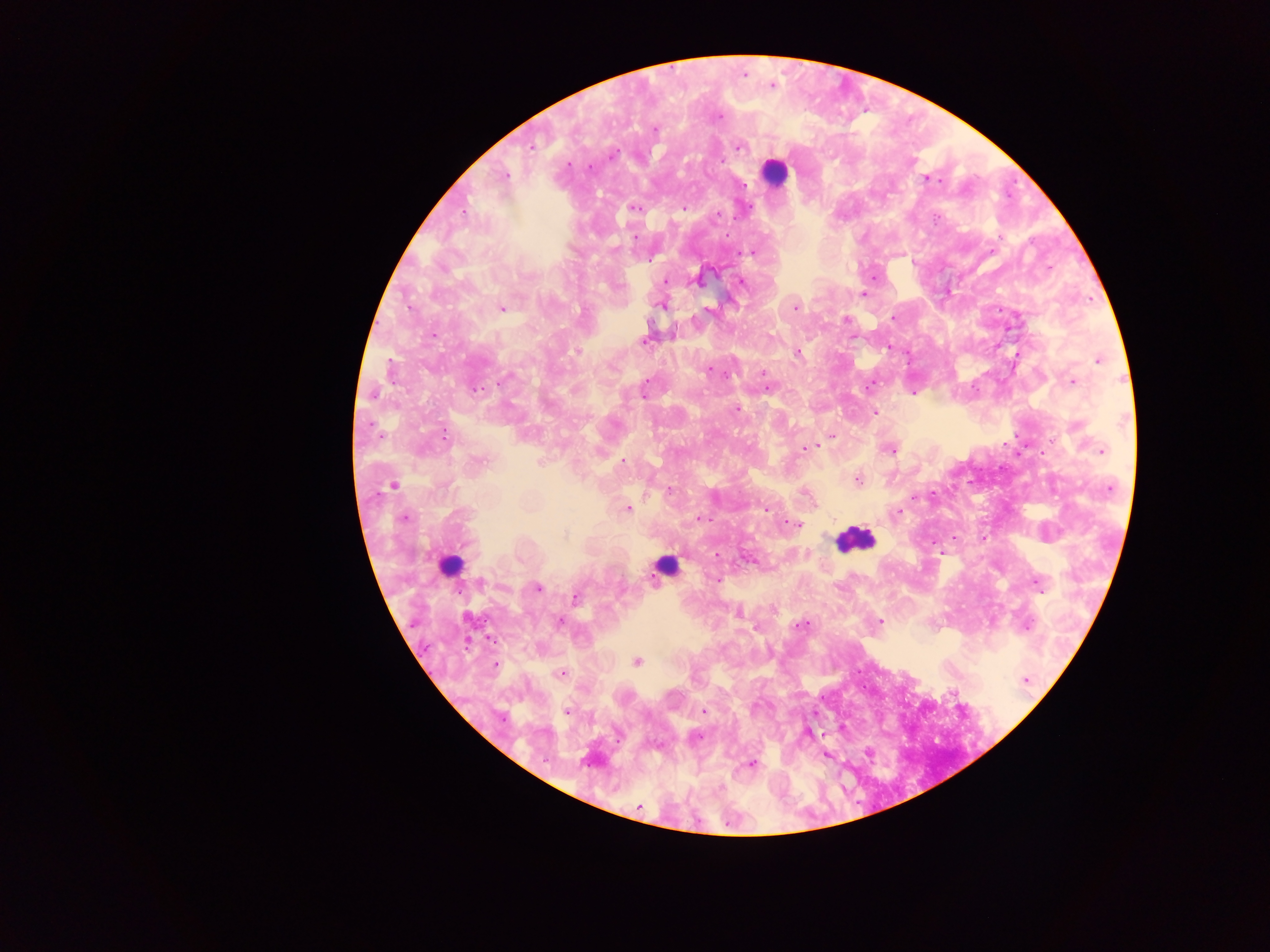
preparation = thick blood film
image size = 1270×952 pixels
field of view = single
country = Ghana
capture = mobile-phone photograph through a microscope
leukocyte locations = approximate centers as (x, y) in pixels: (774, 171), (856, 538), (448, 565), (661, 566)
malaria parasite locations = approximate centers as (x, y) in pixels: (743, 74), (772, 85), (716, 116), (655, 129), (531, 145), (738, 146), (611, 155), (721, 159), (568, 164), (502, 176), (926, 178), (634, 207), (684, 208), (634, 236), (750, 251), (874, 277), (698, 278), (664, 280), (741, 281), (862, 293), (662, 303), (795, 307), (502, 308), (708, 310), (845, 320), (432, 334), (646, 338), (888, 346), (577, 350), (797, 353), (1098, 359), (709, 369), (762, 374), (1073, 381), (869, 386), (643, 393), (913, 393), (735, 408), (875, 411), (444, 435), (831, 435), (806, 449), (890, 449), (1102, 450), (623, 460), (478, 462), (541, 462), (857, 479), (393, 485), (627, 508), (766, 509), (898, 512), (404, 518), (699, 518), (789, 521), (796, 524), (564, 535), (954, 536), (982, 538), (932, 543), (937, 549), (717, 579), (1037, 583), (537, 588), (575, 597), (773, 608), (737, 612), (558, 622), (880, 622), (802, 624), (1026, 626), (637, 661), (494, 664), (562, 673), (1025, 680), (703, 710), (567, 711), (806, 733), (867, 752), (826, 754), (751, 763), (639, 806)